Assess this cell for malaria.
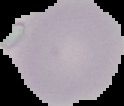

It is uninfected.

image type = segmented cell region on a black background
preparation = thin blood film
image size = 124×106 pixels